Comment on the morphology of the erythrocytes.
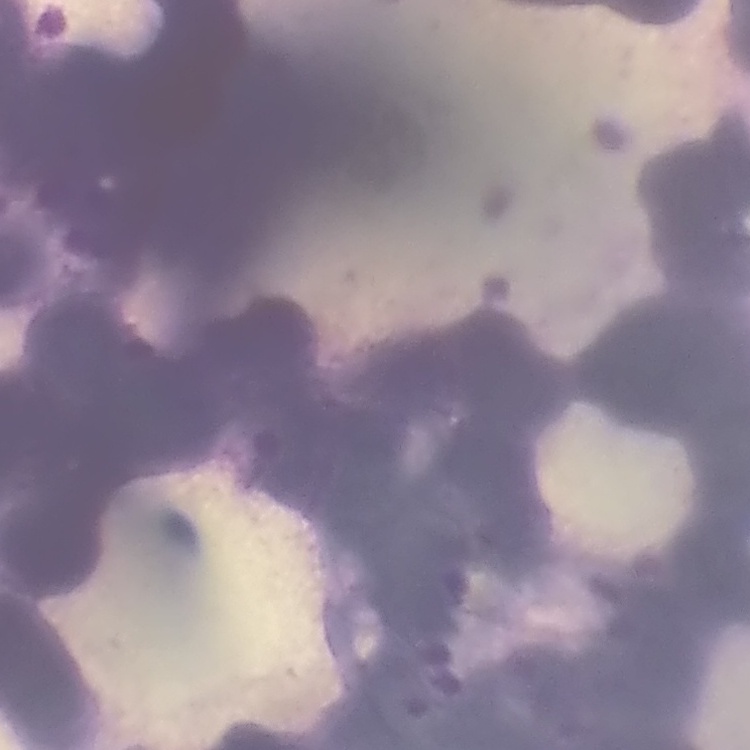
Rouleaux formation.

preparation = thin blood film
stain = Field's or Giemsa
image type = square crop of a larger photomicrograph